Mark where platelets are.
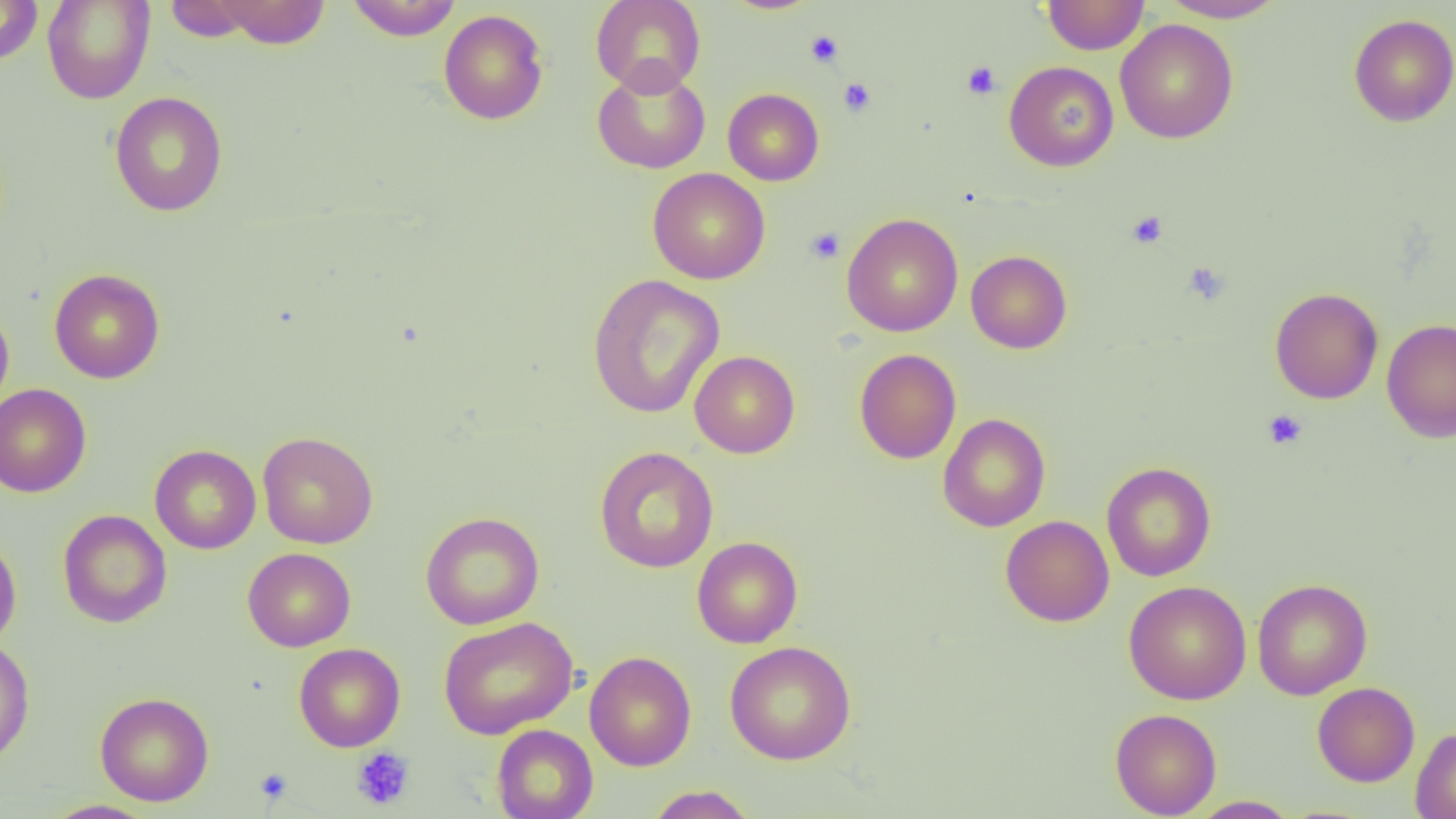
Approximate bounding boxes as named x1/y1/x2/y2 corners in pixels.
Platelets: (x1=805, y1=30, x2=844, y2=67), (x1=962, y1=61, x2=1000, y2=99), (x1=838, y1=78, x2=876, y2=117), (x1=1126, y1=211, x2=1167, y2=249), (x1=805, y1=227, x2=845, y2=264), (x1=1183, y1=262, x2=1229, y2=304), (x1=1262, y1=409, x2=1307, y2=450), (x1=351, y1=747, x2=415, y2=811), (x1=254, y1=769, x2=292, y2=805).

Summary:
  - Uninfected red blood cell locations: (x1=0, y1=0, x2=44, y2=66), (x1=42, y1=0, x2=155, y2=104), (x1=163, y1=0, x2=263, y2=42), (x1=213, y1=0, x2=330, y2=49), (x1=345, y1=0, x2=462, y2=41), (x1=591, y1=0, x2=706, y2=96), (x1=1042, y1=0, x2=1149, y2=55), (x1=1158, y1=0, x2=1289, y2=23), (x1=438, y1=9, x2=549, y2=125), (x1=1348, y1=13, x2=1456, y2=126), (x1=1115, y1=18, x2=1239, y2=144), (x1=1004, y1=61, x2=1118, y2=171), (x1=592, y1=65, x2=710, y2=174), (x1=723, y1=88, x2=824, y2=186), (x1=109, y1=91, x2=229, y2=216), (x1=648, y1=168, x2=770, y2=284), (x1=841, y1=213, x2=963, y2=336), (x1=965, y1=250, x2=1072, y2=353), (x1=49, y1=268, x2=165, y2=383), (x1=587, y1=274, x2=725, y2=419), (x1=1269, y1=286, x2=1384, y2=404), (x1=0, y1=303, x2=14, y2=416), (x1=1382, y1=319, x2=1456, y2=443), (x1=855, y1=348, x2=961, y2=464), (x1=689, y1=351, x2=800, y2=458), (x1=0, y1=383, x2=92, y2=498), (x1=937, y1=413, x2=1050, y2=532), (x1=257, y1=431, x2=378, y2=549), (x1=150, y1=444, x2=261, y2=554), (x1=594, y1=445, x2=719, y2=574), (x1=1101, y1=462, x2=1216, y2=581), (x1=58, y1=509, x2=172, y2=628), (x1=420, y1=511, x2=544, y2=630), (x1=1000, y1=515, x2=1114, y2=626), (x1=0, y1=532, x2=22, y2=652), (x1=691, y1=536, x2=803, y2=648), (x1=242, y1=547, x2=356, y2=651), (x1=1252, y1=578, x2=1373, y2=700), (x1=1123, y1=581, x2=1251, y2=705), (x1=438, y1=616, x2=578, y2=739), (x1=0, y1=636, x2=35, y2=767), (x1=724, y1=640, x2=856, y2=765), (x1=294, y1=642, x2=406, y2=752), (x1=584, y1=651, x2=697, y2=771), (x1=1312, y1=681, x2=1420, y2=787), (x1=95, y1=691, x2=214, y2=806), (x1=1110, y1=708, x2=1222, y2=818), (x1=491, y1=724, x2=598, y2=819), (x1=1410, y1=727, x2=1456, y2=818), (x1=645, y1=785, x2=758, y2=819), (x1=1186, y1=796, x2=1303, y2=818), (x1=42, y1=800, x2=158, y2=819)
  - Slide-level diagnosis: no evidence of blood parasites
  - Image size: 1456×819 pixels
  - Preparation: thin blood film
  - Modality: optical microscopy
  - Field of view: single
  - Magnification: 1000x